Assess this cell for malaria.
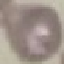
It is uninfected.

Summary:
  - Preparation: thin blood smear
  - Capture: smartphone through the microscope eyepiece
  - Stain: Giemsa
  - Image type: cell patch, automatically extracted from a larger field of view and resized to 64 × 64 pixels